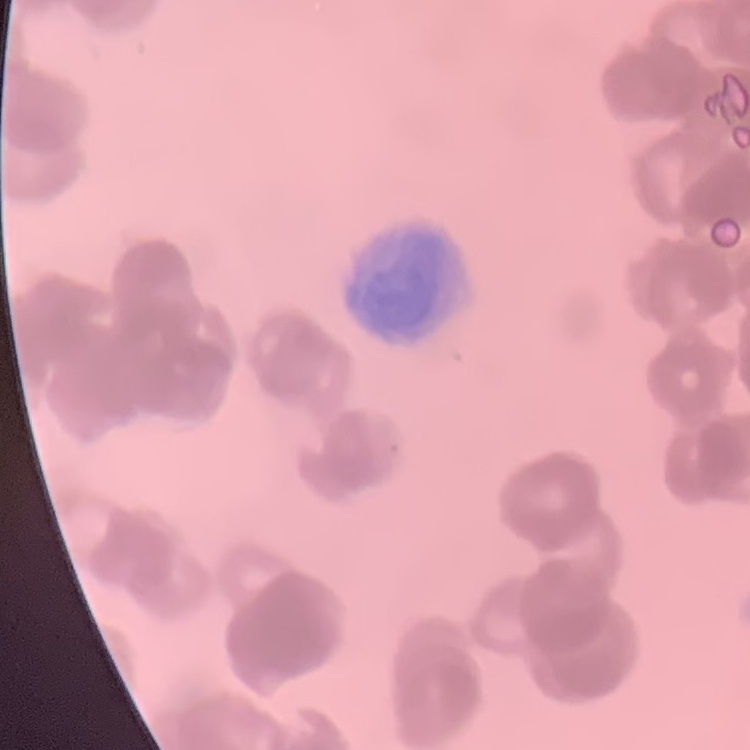 The red blood cells show rouleaux formation. Field's or Giemsa stain. Thin peripheral smear. Square crop of a larger photomicrograph.